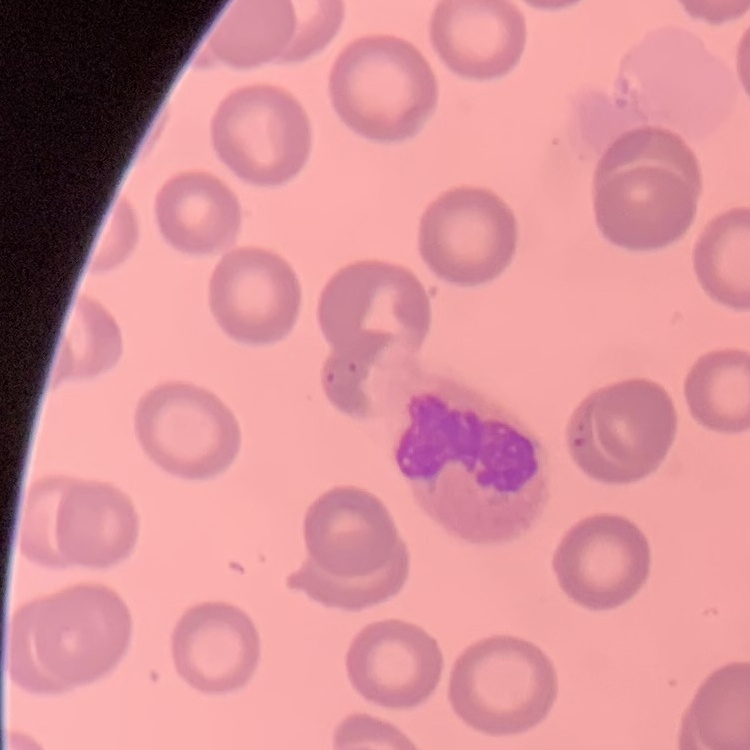

The red blood cells exhibit no rouleaux formation. Thin peripheral smear. Stained with either Field's or Giemsa. Square crop of a larger photomicrograph.